Report the malaria status of this cell.
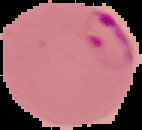
It is parasitized.

image type = cell region segmented out of the field of view; surrounding area masked to black
preparation = thin blood smear
image size = 142×130 pixels